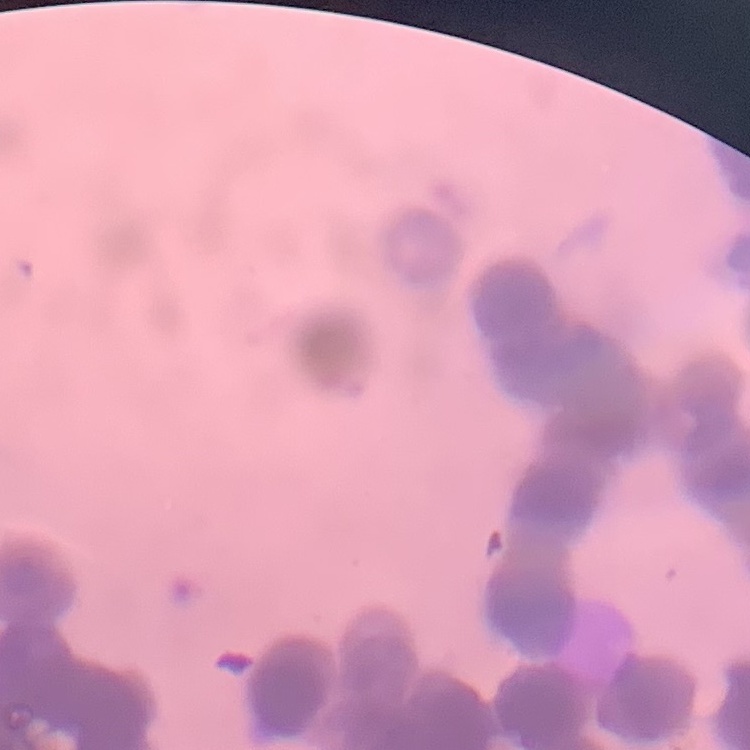
Summary:
  - Erythrocyte morphology: rouleaux formation
  - Image type: square crop of a larger photomicrograph
  - Preparation: thin peripheral smear
  - Stain: Field's or Giemsa